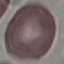

result: negative for malaria parasites
preparation: thin smear
stain: Giemsa
capture: smartphone through the microscope eyepiece
image_type: cell patch, automatically extracted from a larger field of view and resized to 64 × 64 pixels